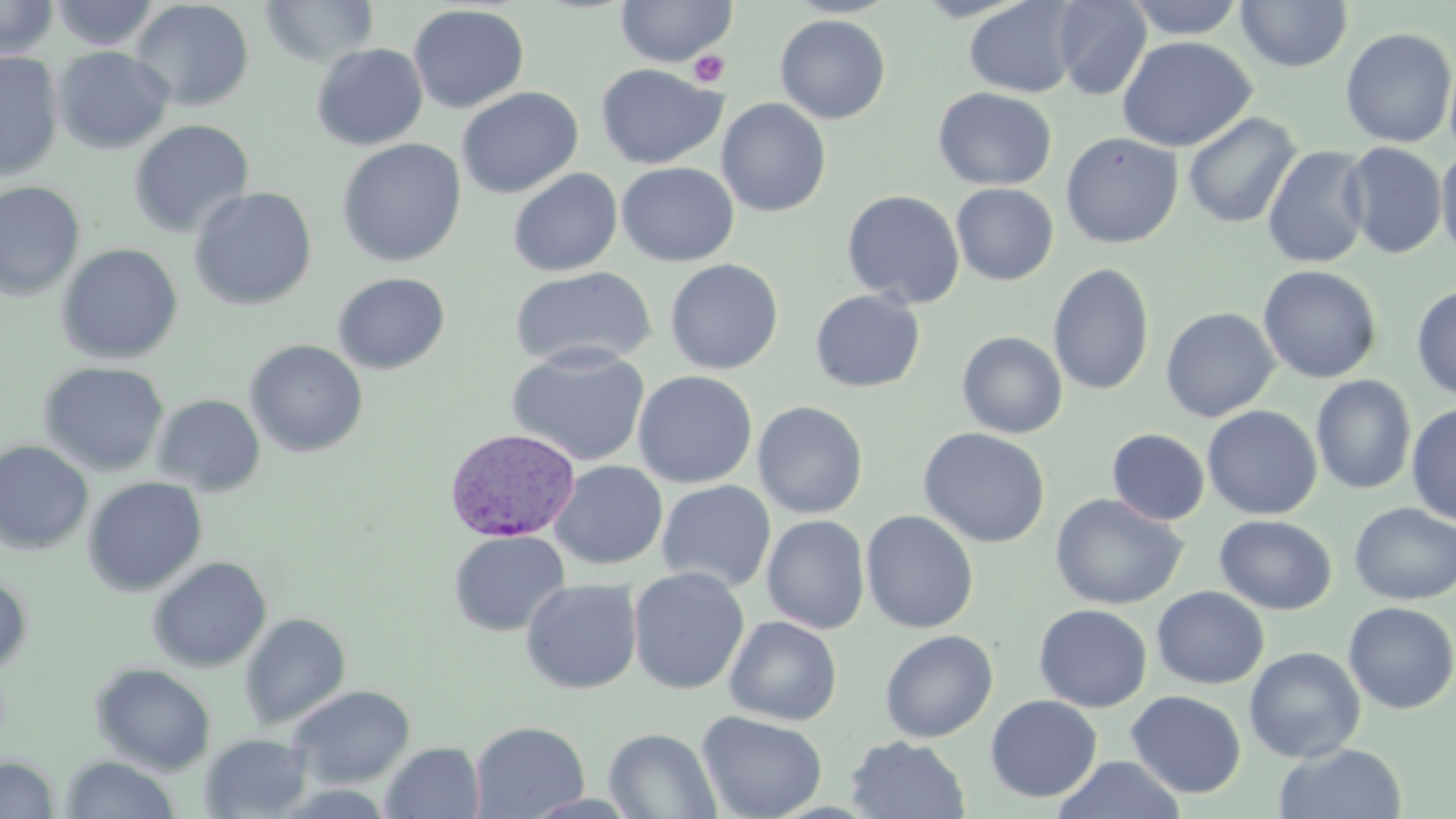
Summary:
  - Coordinate format: approximate bounding boxes as (x1, y1, x2, y2) in pixels
  - Uninfected red blood cell locations: (0, 0, 59, 59), (258, 0, 380, 68), (614, 0, 739, 67), (1122, 0, 1248, 39), (49, 1, 161, 51), (130, 1, 255, 112), (963, 1, 1083, 98), (1050, 1, 1151, 101), (1236, 1, 1353, 72), (408, 4, 530, 113), (775, 14, 891, 124), (1340, 26, 1456, 148), (1116, 36, 1256, 152), (311, 43, 428, 150), (52, 46, 174, 154), (0, 52, 63, 182), (1444, 53, 1456, 164), (596, 64, 726, 169), (456, 87, 584, 199), (932, 87, 1057, 191), (716, 98, 832, 217), (1182, 112, 1302, 229), (128, 119, 255, 239), (1060, 132, 1184, 249), (337, 138, 467, 267), (1340, 142, 1448, 260), (1261, 145, 1373, 269), (1436, 146, 1456, 265), (617, 162, 739, 266), (507, 168, 623, 277), (0, 181, 85, 301), (951, 183, 1059, 285), (188, 186, 317, 311), (842, 189, 965, 308), (56, 243, 184, 365), (664, 258, 784, 375), (1048, 262, 1156, 396), (1258, 264, 1382, 384), (509, 267, 657, 370), (332, 272, 450, 375), (1411, 284, 1456, 400), (809, 289, 926, 393), (1160, 306, 1281, 422), (956, 331, 1068, 439), (244, 339, 368, 457), (506, 345, 651, 468), (38, 361, 171, 478), (632, 370, 757, 488), (1311, 375, 1417, 495), (152, 394, 266, 496), (753, 400, 868, 519), (1406, 403, 1456, 526), (1202, 405, 1322, 520), (917, 427, 1051, 548), (1106, 428, 1210, 526), (0, 441, 94, 555), (550, 460, 667, 569), (82, 476, 208, 597), (656, 480, 776, 593), (1050, 493, 1188, 610), (1349, 502, 1456, 606), (860, 510, 979, 634), (762, 514, 870, 634), (1214, 514, 1337, 615), (448, 530, 570, 637), (147, 555, 272, 673), (628, 566, 750, 695), (0, 573, 33, 677), (520, 578, 642, 694), (1151, 586, 1269, 689), (1342, 601, 1456, 714), (1034, 604, 1153, 712), (239, 612, 351, 730), (723, 616, 842, 725), (880, 630, 998, 743), (1244, 646, 1366, 763), (91, 663, 216, 775), (287, 685, 416, 788), (1126, 690, 1247, 798), (985, 694, 1103, 803), (697, 710, 828, 819), (470, 720, 590, 818), (604, 728, 721, 818), (199, 732, 314, 818), (845, 735, 971, 818), (381, 741, 485, 818), (1274, 743, 1408, 819), (61, 754, 180, 818), (1054, 755, 1185, 818), (0, 756, 58, 819)
  - Platelet locations: (689, 51, 729, 88)
  - Plasmodium vivax-infected red blood cell locations: (444, 428, 582, 542)
  - Slide-level diagnosis: Plasmodium vivax
  - Modality: optical microscopy
  - Field of view: single
  - Magnification: 1000x
  - Preparation: thin blood film
  - Image size: 1456×819 pixels
  - Stain: May-Grünwald-Giemsa